Assess the morphology of the red blood cells.
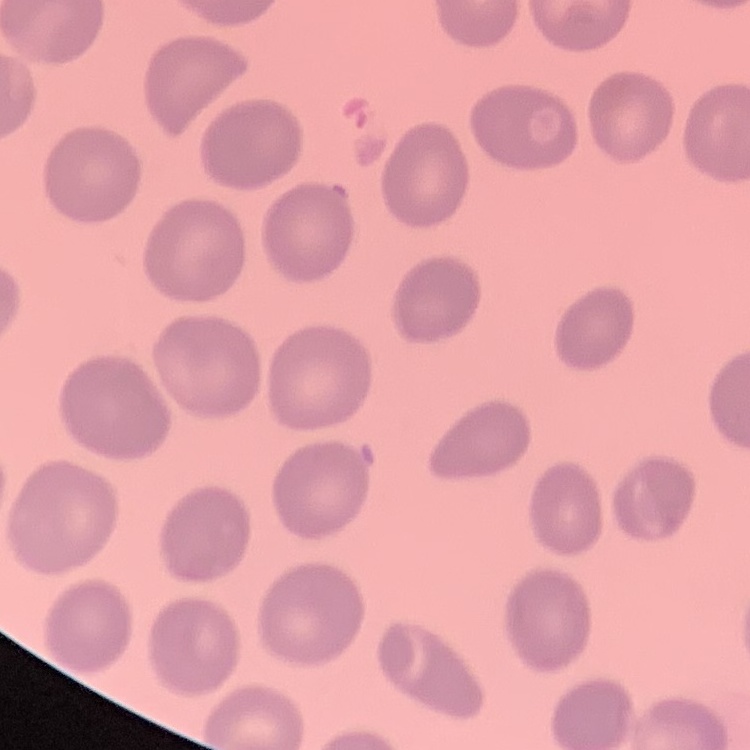

No rouleaux formation.

Summary:
  - Image type: square crop of a larger photomicrograph
  - Stain: Field's or Giemsa
  - Preparation: thin peripheral smear